Name the blood parasite species.
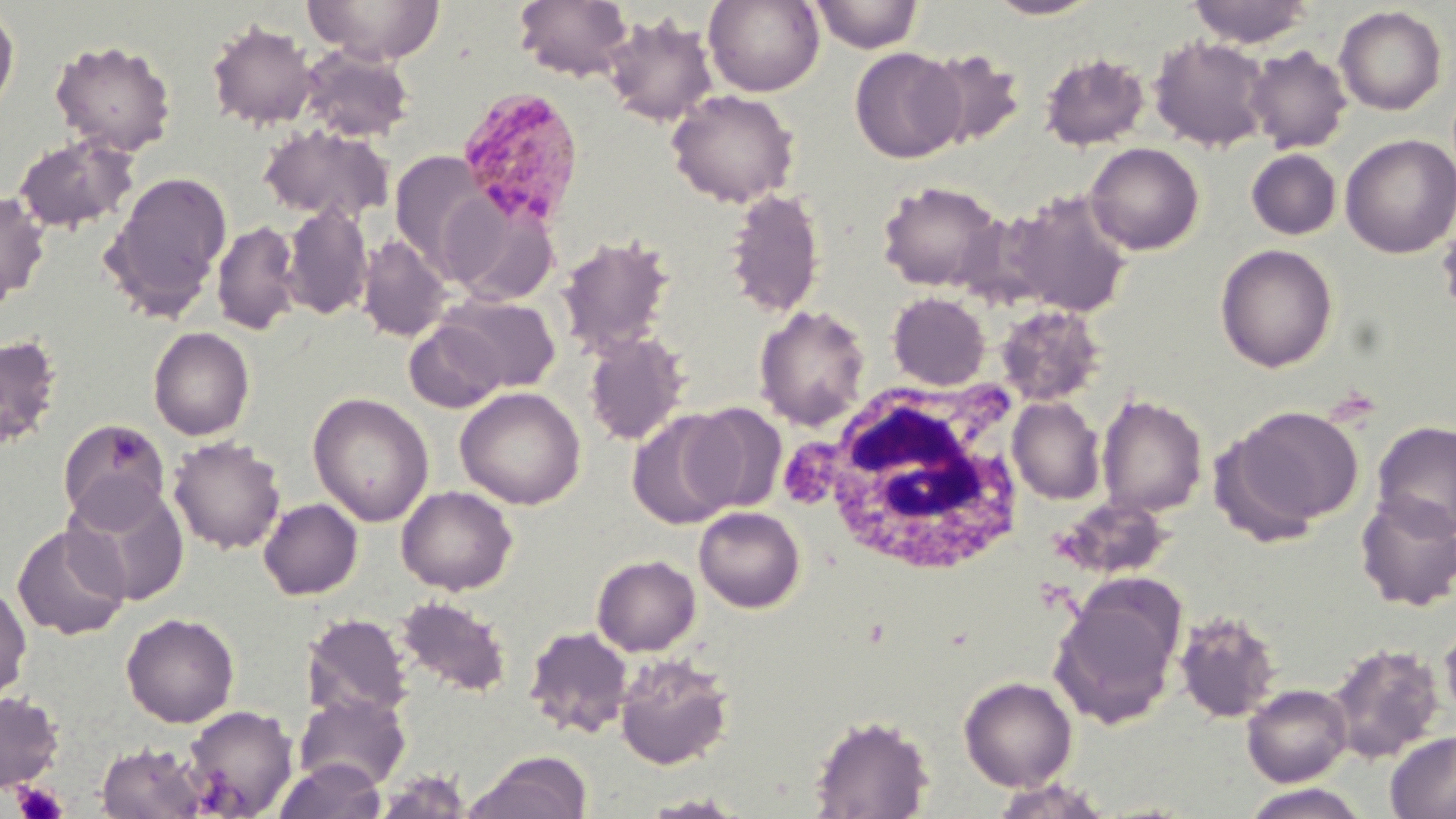

Plasmodium malariae.

{
  "field_of_view": "single",
  "plasmodium_malariae_infected_red_blood_cell_locations": "approximate bounding boxes as (x1,y1)-(x2,y2) corner pairs in pixels: (454,86)-(586,231)",
  "modality": "optical microscopy",
  "stain": "May-Grünwald-Giemsa",
  "magnification": "1000x",
  "platelet_locations": "approximate bounding boxes as (x1,y1)-(x2,y2) corner pairs in pixels: (12,782)-(69,819)",
  "white_blood_cell_locations": "approximate bounding boxes as (x1,y1)-(x2,y2) corner pairs in pixels: (798,379)-(1034,581)",
  "uninfected_red_blood_cell_locations": "approximate bounding boxes as (x1,y1)-(x2,y2) corner pairs in pixels: (305,0)-(445,64), (514,0)-(633,81), (704,0)-(824,96), (809,0)-(924,53), (986,0)-(1101,20), (1187,0)-(1314,48), (0,3)-(20,122), (1334,5)-(1447,115), (602,12)-(719,126), (206,20)-(318,129), (1149,34)-(1272,152), (50,38)-(177,156), (1245,45)-(1352,154), (299,46)-(415,142), (849,47)-(966,163), (919,48)-(1026,149), (1039,52)-(1150,151), (667,89)-(799,207), (259,124)-(394,224), (12,133)-(138,234), (1339,133)-(1456,258), (1085,142)-(1205,255), (1246,148)-(1342,240), (389,150)-(490,274), (101,169)-(233,319), (877,180)-(1004,292), (724,187)-(826,318), (1002,189)-(1133,318), (0,190)-(50,307), (441,192)-(560,307), (281,203)-(373,320), (212,220)-(302,336), (557,234)-(675,358), (357,235)-(451,342), (1215,243)-(1338,373), (887,292)-(990,390), (437,294)-(561,394), (753,304)-(870,430), (995,304)-(1106,406), (404,320)-(508,413), (149,326)-(255,440), (583,331)-(689,446), (0,334)-(63,449), (455,386)-(586,510), (308,392)-(433,527), (1096,394)-(1208,518), (1007,397)-(1105,505), (684,403)-(786,513), (1227,405)-(1364,532), (627,410)-(739,530), (57,419)-(171,529), (1371,421)-(1456,538), (168,435)-(285,555), (63,481)-(190,606), (396,485)-(518,595), (1355,491)-(1456,611), (1054,496)-(1174,580), (259,498)-(362,600), (694,506)-(805,613), (12,523)-(130,640), (592,554)-(700,656), (0,580)-(32,702), (1050,582)-(1185,729), (395,595)-(513,697), (1173,608)-(1283,723), (121,612)-(240,727), (301,613)-(413,721), (1439,614)-(1456,727), (524,626)-(633,739), (1325,642)-(1446,763), (613,653)-(735,771), (959,675)-(1077,791), (1242,684)-(1352,786), (0,691)-(64,792), (293,693)-(411,791), (182,704)-(298,817), (809,714)-(935,819), (1385,732)-(1456,818), (96,742)-(209,819), (465,751)-(592,819), (273,758)-(386,819), (374,772)-(473,818), (989,778)-(1115,819), (1238,784)-(1373,819), (639,794)-(748,818)",
  "preparation": "thin blood film",
  "image_size": "1456×819 pixels"
}